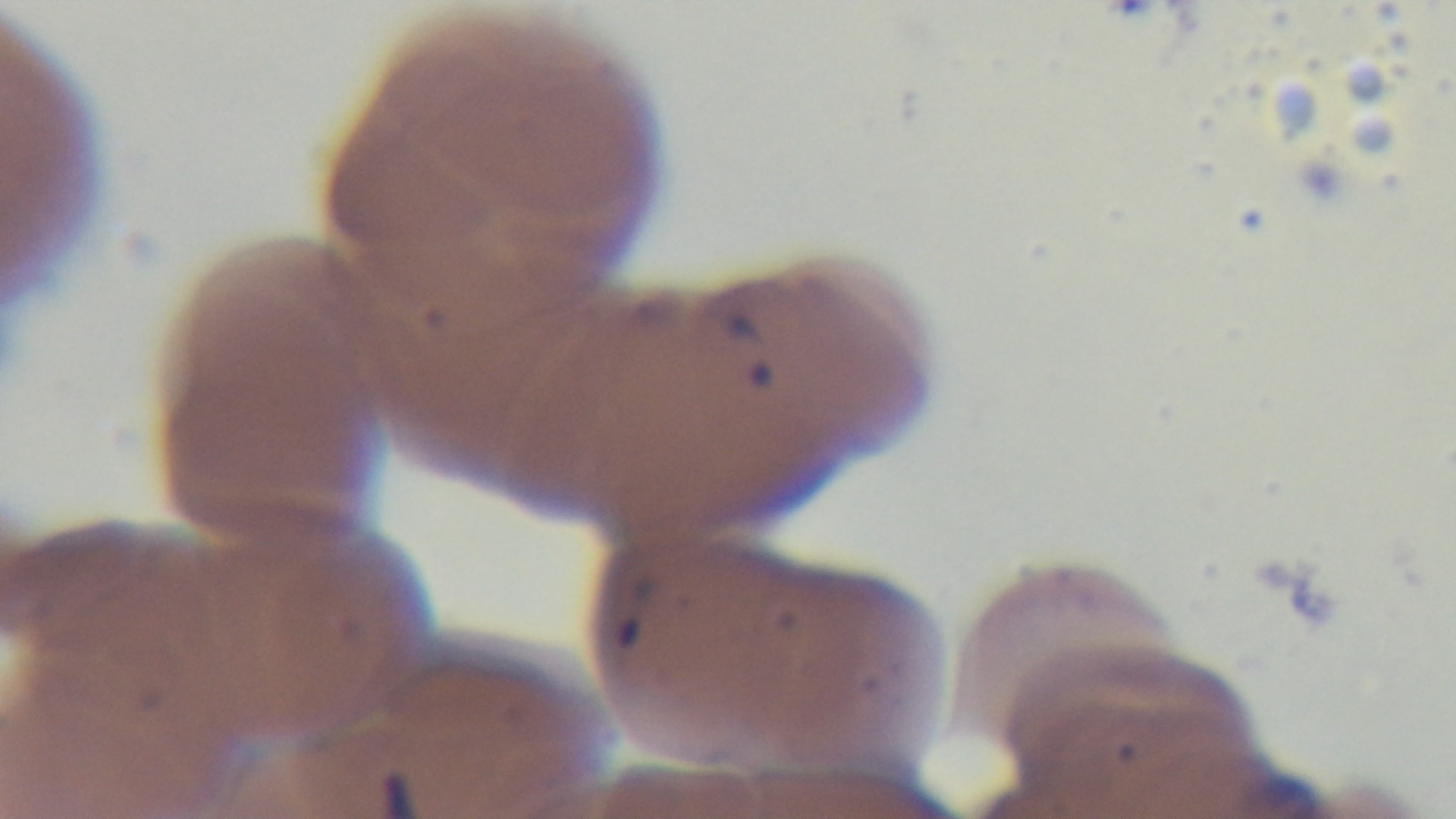

One field from the slide. Giemsa-stained. Photomicrograph. Oil-immersion objective, 100x. Mounted 4K digital camera. Preparation: thin blood film. Malaria status: infected.